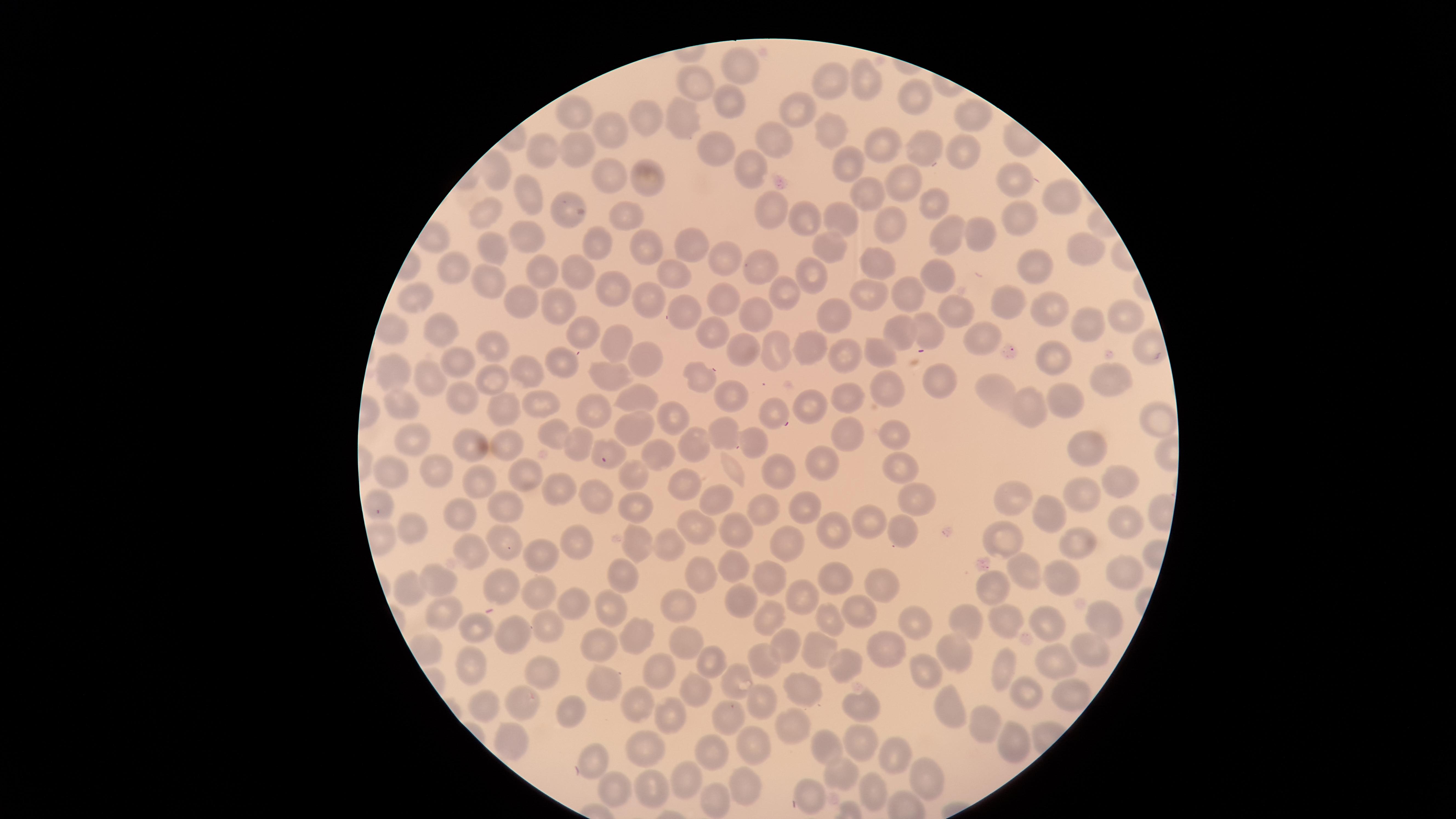
Approximate marker points, in pixels from the top-left corner. Uninfected red blood cells: (x=745, y=69), (x=827, y=80), (x=868, y=82), (x=693, y=86), (x=911, y=95), (x=731, y=100), (x=794, y=112), (x=652, y=115), (x=579, y=116), (x=976, y=118), (x=689, y=123), (x=611, y=130), (x=829, y=136), (x=771, y=138), (x=542, y=146), (x=878, y=146), (x=923, y=148), (x=578, y=149), (x=720, y=151), (x=962, y=155), (x=845, y=160), (x=741, y=166), (x=493, y=168), (x=607, y=173), (x=646, y=180), (x=900, y=182), (x=1014, y=182), (x=864, y=191), (x=526, y=195), (x=1059, y=199), (x=929, y=204), (x=773, y=208), (x=573, y=210), (x=488, y=218), (x=839, y=218), (x=1019, y=218), (x=625, y=219), (x=808, y=222), (x=883, y=226), (x=979, y=231), (x=944, y=234), (x=529, y=238), (x=829, y=243), (x=601, y=246), (x=1085, y=249), (x=491, y=250), (x=693, y=250), (x=643, y=252), (x=729, y=260), (x=1035, y=263), (x=874, y=264), (x=764, y=265), (x=574, y=270), (x=460, y=271), (x=540, y=271), (x=811, y=273), (x=679, y=274), (x=947, y=275), (x=491, y=284), (x=607, y=286), (x=784, y=296), (x=902, y=296), (x=1012, y=297), (x=413, y=298), (x=521, y=298), (x=859, y=298), (x=649, y=301), (x=725, y=304), (x=558, y=307), (x=690, y=310), (x=953, y=311), (x=1045, y=311), (x=757, y=316), (x=831, y=316), (x=1123, y=318), (x=444, y=325), (x=1082, y=325), (x=928, y=326), (x=581, y=329), (x=707, y=330), (x=979, y=333), (x=897, y=335), (x=607, y=344), (x=740, y=345), (x=497, y=346), (x=1149, y=348), (x=812, y=349), (x=770, y=351), (x=875, y=355), (x=643, y=356), (x=844, y=356), (x=562, y=361), (x=1058, y=361), (x=460, y=364), (x=524, y=370), (x=394, y=371), (x=609, y=374), (x=697, y=376), (x=943, y=378), (x=423, y=379), (x=1115, y=379), (x=492, y=380), (x=893, y=388), (x=846, y=392), (x=461, y=395), (x=1001, y=395), (x=631, y=397), (x=729, y=397), (x=1061, y=402), (x=399, y=405), (x=812, y=405), (x=540, y=407), (x=504, y=410), (x=1032, y=410), (x=776, y=412), (x=589, y=414), (x=672, y=418), (x=1157, y=421), (x=634, y=428), (x=845, y=434), (x=553, y=435), (x=722, y=435), (x=896, y=438), (x=415, y=440), (x=576, y=443), (x=749, y=444), (x=506, y=446), (x=609, y=447), (x=469, y=448), (x=693, y=448), (x=1084, y=452), (x=656, y=454), (x=827, y=460), (x=895, y=467), (x=440, y=471), (x=731, y=471), (x=525, y=474), (x=386, y=476), (x=772, y=477), (x=636, y=478), (x=685, y=482), (x=479, y=483), (x=1119, y=484), (x=559, y=488), (x=913, y=496), (x=1016, y=497), (x=1078, y=498), (x=593, y=502), (x=716, y=502), (x=377, y=505), (x=636, y=507), (x=801, y=507), (x=506, y=511), (x=762, y=513), (x=1049, y=516), (x=459, y=518), (x=1118, y=519), (x=696, y=522), (x=872, y=522), (x=830, y=528), (x=730, y=530), (x=408, y=531), (x=902, y=532), (x=1005, y=539), (x=505, y=543), (x=638, y=543), (x=582, y=545), (x=673, y=545), (x=789, y=545), (x=1079, y=545), (x=474, y=553), (x=546, y=555), (x=736, y=567), (x=1121, y=568), (x=1025, y=570), (x=769, y=573), (x=620, y=579), (x=1067, y=579), (x=698, y=580), (x=439, y=582), (x=830, y=582), (x=500, y=584), (x=875, y=585), (x=992, y=591), (x=409, y=593), (x=537, y=595), (x=801, y=597), (x=612, y=602), (x=577, y=604), (x=740, y=604), (x=682, y=607), (x=445, y=613), (x=862, y=613), (x=1101, y=617), (x=769, y=620), (x=918, y=621), (x=1043, y=621), (x=969, y=622), (x=999, y=622), (x=832, y=623), (x=544, y=627), (x=475, y=628), (x=511, y=633), (x=633, y=636), (x=884, y=643), (x=603, y=644), (x=681, y=645), (x=1083, y=645), (x=789, y=647), (x=819, y=652), (x=956, y=657), (x=708, y=661), (x=1053, y=661), (x=767, y=662), (x=470, y=664), (x=845, y=666), (x=543, y=669), (x=658, y=671), (x=926, y=671), (x=1004, y=674), (x=734, y=681), (x=596, y=686), (x=691, y=686), (x=799, y=691), (x=1024, y=692), (x=1069, y=694), (x=483, y=702), (x=523, y=704), (x=765, y=706), (x=863, y=707), (x=946, y=709), (x=569, y=711), (x=641, y=712), (x=726, y=718), (x=672, y=720), (x=981, y=725), (x=789, y=728), (x=512, y=741), (x=644, y=745), (x=861, y=745), (x=1007, y=745), (x=756, y=747), (x=829, y=747), (x=707, y=752), (x=892, y=755), (x=590, y=759), (x=683, y=775), (x=925, y=776), (x=838, y=777), (x=747, y=784), (x=808, y=791), (x=653, y=792), (x=615, y=793), (x=715, y=794), (x=875, y=794). Giemsa-stained preparation. Thin blood film. Image is 1456×819 pixels. One field of view of the specimen. Circular visible region. Smartphone photograph through the microscope eyepiece. Presence: no malaria parasites identified.